Report the malaria status of this cell.
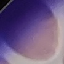

It is uninfected.

Giemsa-stained preparation. Photographed with a smartphone camera at the microscope eyepiece. Thin smear of blood. Cell patch, automatically extracted from a larger field of view and resized to 64 × 64 pixels.